Name the parasite shown.
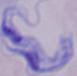
This is a trypanosome.

Summary:
  - Modality: micrograph
  - Magnification: 1000x